Assess this cell for malaria.
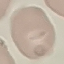
Uninfected.

{
  "capture": "smartphone through the microscope eyepiece",
  "preparation": "thin blood film",
  "image_type": "cell patch, automatically extracted from a larger field of view and resized to 64 × 64 pixels",
  "stain": "Giemsa"
}